State which parasite is depicted.
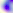
Toxoplasma gondii.

Summary:
  - Magnification: 400x
  - Modality: photomicrograph